Name the parasite shown.
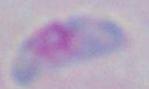

Toxoplasma gondii.

Photomicrograph. 1000x magnification.